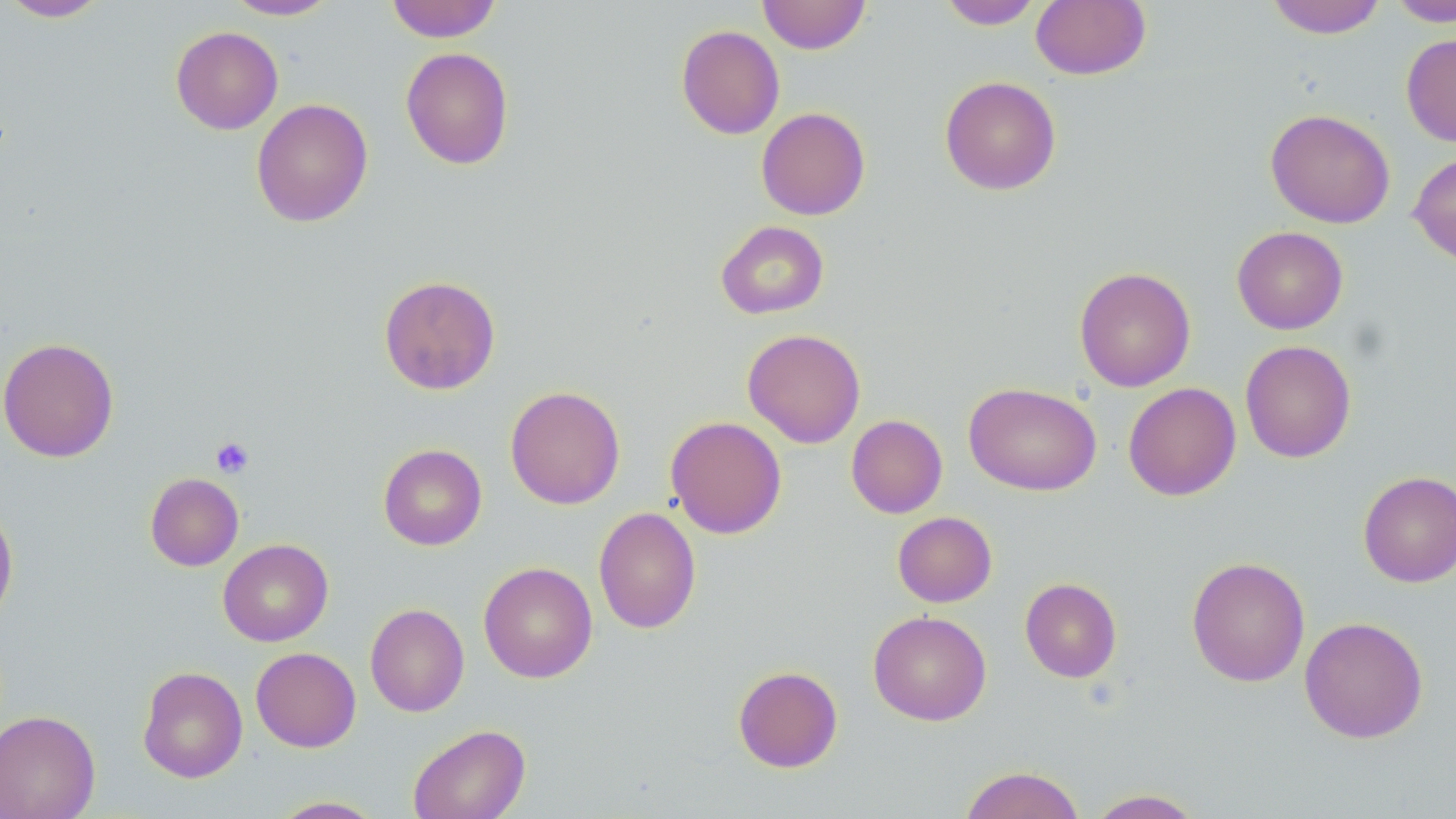

Approximate bounding boxes as (x1,y1)-(x2,y2) corner pairs in pixels. Platelet locations: (211,437)-(254,478). Uninfected red blood cell locations: (1,0)-(114,22), (223,0)-(339,20), (386,0)-(502,42), (758,0)-(871,54), (937,0)-(1043,29), (1265,0)-(1388,38), (1386,0)-(1456,27), (1030,1)-(1151,80), (676,24)-(785,139), (171,26)-(283,134), (1401,34)-(1456,147), (401,47)-(514,170), (939,76)-(1061,195), (251,98)-(374,227), (756,106)-(871,220), (1265,108)-(1395,228), (1408,151)-(1456,267), (715,220)-(829,320), (1232,226)-(1348,334), (1074,266)-(1196,392), (379,275)-(501,395), (742,328)-(866,448), (0,337)-(120,463), (1240,340)-(1357,463), (963,382)-(1102,496), (1123,382)-(1241,501), (505,385)-(625,509), (846,414)-(947,518), (665,415)-(787,539), (378,443)-(487,550), (1358,470)-(1456,587), (145,472)-(244,571), (0,500)-(19,629), (593,506)-(701,634), (892,511)-(997,607), (218,539)-(333,647), (1187,556)-(1310,687), (478,561)-(598,682), (1020,577)-(1122,682), (365,603)-(469,717), (868,610)-(992,725), (1299,615)-(1428,743), (251,647)-(361,752), (732,665)-(843,772), (138,666)-(248,783), (0,710)-(101,819), (407,723)-(531,819), (959,765)-(1086,819), (1086,788)-(1205,818), (270,796)-(387,818). Slide-level diagnosis: negative for blood parasites. Single field of view. Captured at 1000x magnification. Thin blood smear. May-Grünwald-Giemsa stain. Image is 1456×819 pixels. Optical microscopy.